State the preparation type.
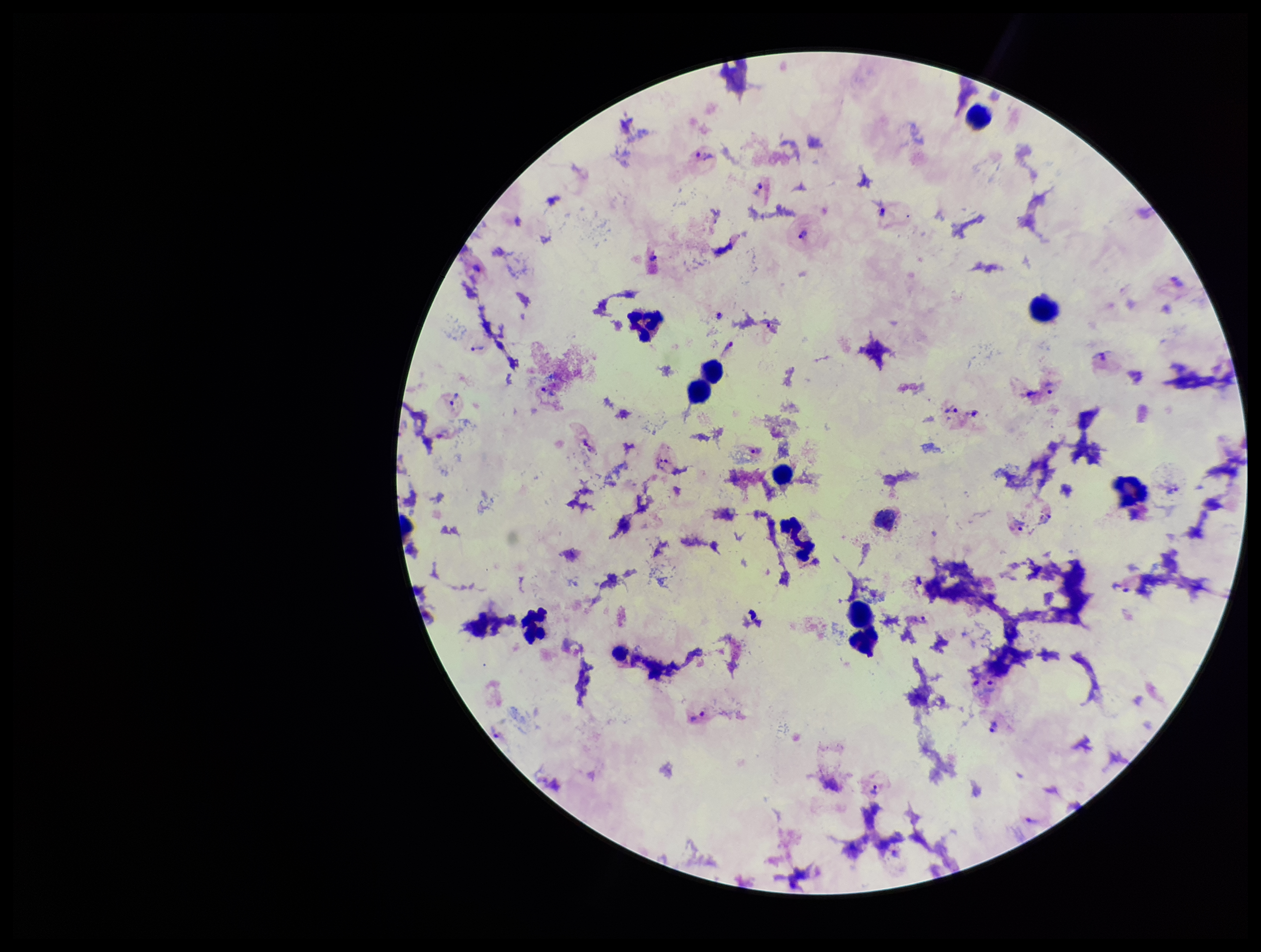
Thick.

parasite count = 20
image size = 1261×952 pixels
patient malaria status = positive
field of view = single
stain = Giemsa
capture = smartphone photograph through the microscope eyepiece
leukocyte count = 13
Plasmodium parasites = detected
species reported for this patient = Plasmodium vivax